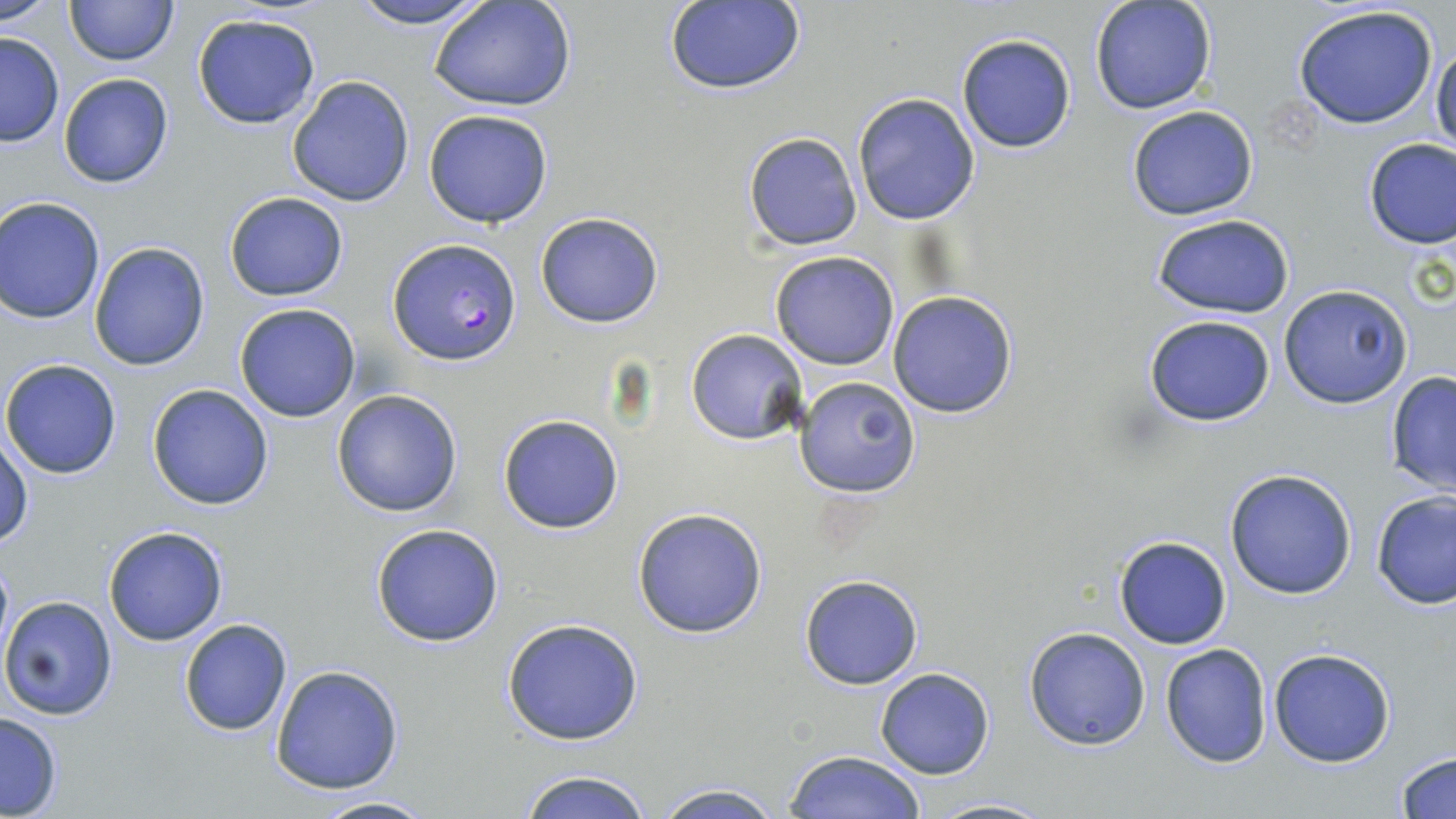 Approximate bounding boxes as (x1,y1)-(x2,y2) corner pairs in pixels. Uninfected red blood cell locations: (0,0)-(62,24), (64,0)-(178,66), (348,0)-(493,29), (428,0)-(577,113), (1089,1)-(1218,115), (662,2)-(806,95), (1292,3)-(1441,130), (191,13)-(321,130), (0,32)-(65,147), (955,33)-(1076,154), (1431,40)-(1456,155), (57,72)-(176,189), (286,75)-(416,207), (852,93)-(980,225), (1126,104)-(1260,221), (423,108)-(554,228), (742,131)-(863,251), (1362,137)-(1456,249), (224,191)-(350,302), (1,199)-(105,323), (535,211)-(662,328), (1150,213)-(1295,317), (87,241)-(211,372), (770,251)-(899,370), (1280,283)-(1411,408), (887,290)-(1018,417), (234,303)-(361,423), (1143,315)-(1277,425), (686,329)-(810,445), (1,358)-(122,479), (1385,371)-(1456,496), (796,375)-(918,497), (147,383)-(275,511), (331,388)-(464,517), (499,414)-(623,534), (1,432)-(33,549), (1225,468)-(1358,599), (1371,491)-(1456,609), (632,506)-(769,639), (371,523)-(505,646), (103,526)-(229,646), (1113,534)-(1232,649), (799,573)-(924,691), (1,595)-(117,720), (501,617)-(643,745), (179,618)-(294,737), (1023,626)-(1151,750), (1160,643)-(1272,767), (1267,647)-(1396,768), (270,665)-(404,793), (876,667)-(995,779), (0,711)-(64,816), (785,749)-(928,819), (1394,749)-(1456,819), (516,768)-(655,819), (648,782)-(786,819), (307,793)-(440,819), (922,795)-(1056,818). Plasmodium falciparum-infected red blood cell locations: (387,237)-(520,365). Slide-level diagnosis: Plasmodium falciparum. Image is 1456×819 pixels. Single field of view. Optical microscopy. May-Grünwald-Giemsa stain. Captured at 1000x magnification. Thin blood smear.